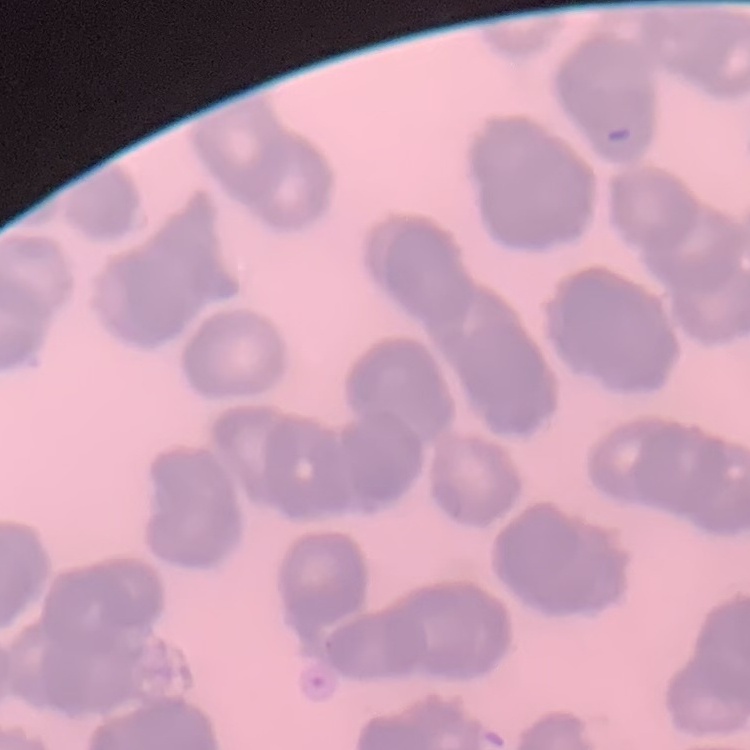

red blood cell morphology = rouleaux formation
preparation = thin peripheral smear
stain = Field's or Giemsa
image type = square crop of a larger photomicrograph